Comment on the morphology of the erythrocytes.
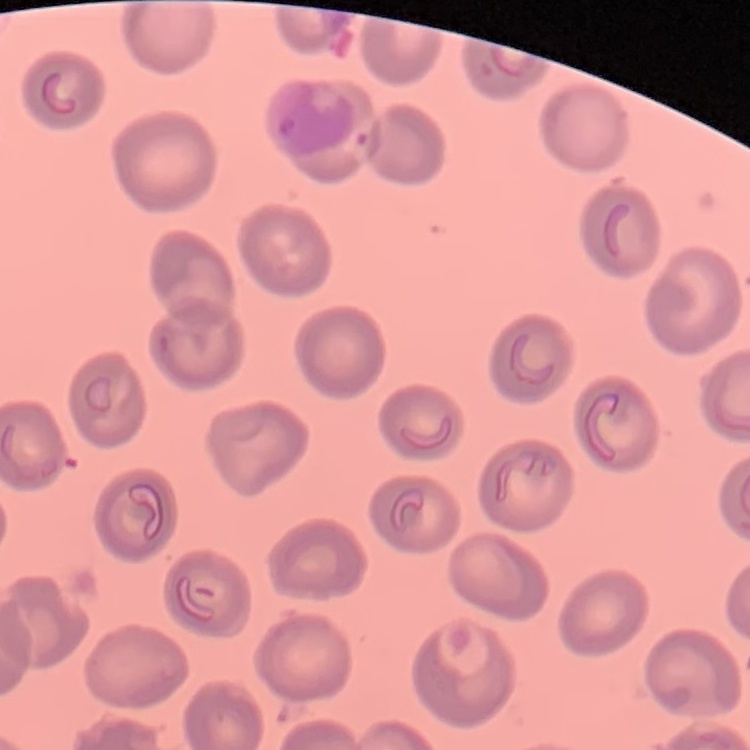
They show no rouleaux formation.

Summary:
  - Image type: square crop of a larger photomicrograph
  - Preparation: thin blood smear
  - Stain: Field's or Giemsa